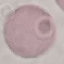
Summary:
  - Result: no malaria parasites detected
  - Image type: cell patch, automatically extracted from a larger field of view and resized to 64 × 64 pixels
  - Preparation: thin smear
  - Capture: smartphone through the microscope eyepiece
  - Stain: Giemsa